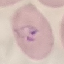
Summary:
  - Result: malaria parasites detected
  - Preparation: thin blood film
  - Stain: Giemsa
  - Capture: smartphone camera at the microscope eyepiece
  - Image type: cell patch, automatically extracted from a larger field of view and resized to 64 × 64 pixels